Assess the morphology of the red blood cells.
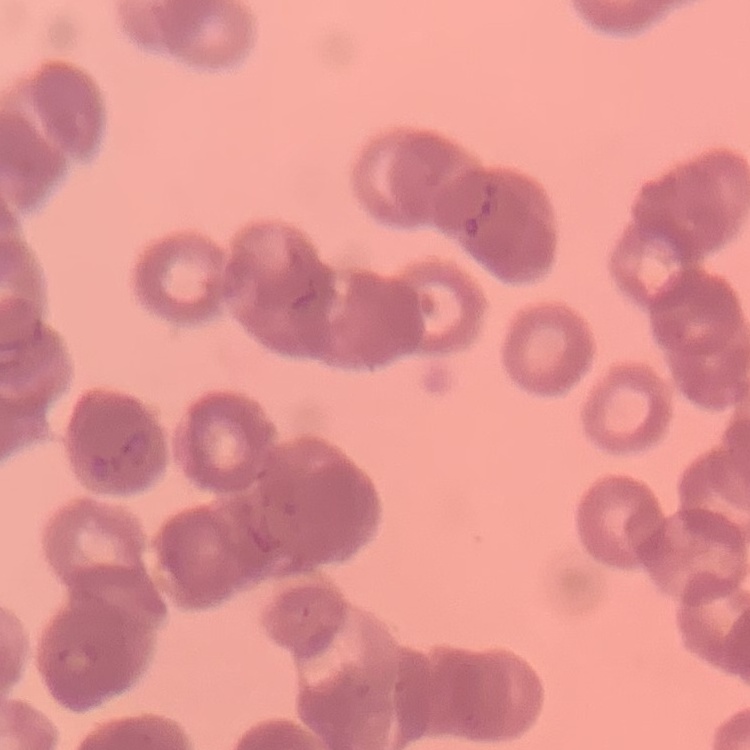

They show rouleaux formation.

Summary:
  - Image type: square crop of a larger photomicrograph
  - Stain: Field's or Giemsa
  - Preparation: thin blood smear